Assess the morphology of the erythrocytes.
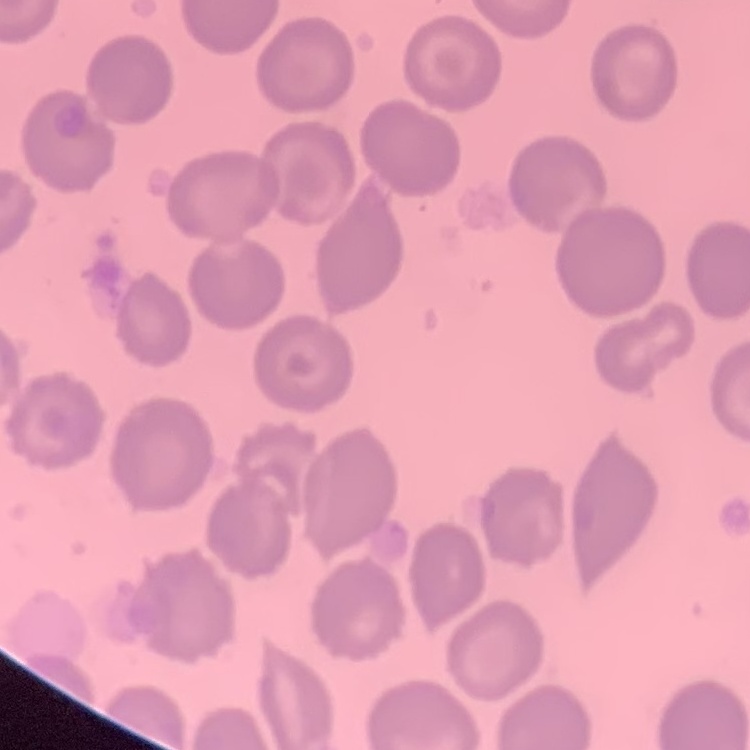

No rouleaux formation.

Thin blood smear. Field's or Giemsa stain. One tile cut from a larger photomicrograph.